Describe the morphology of the erythrocytes.
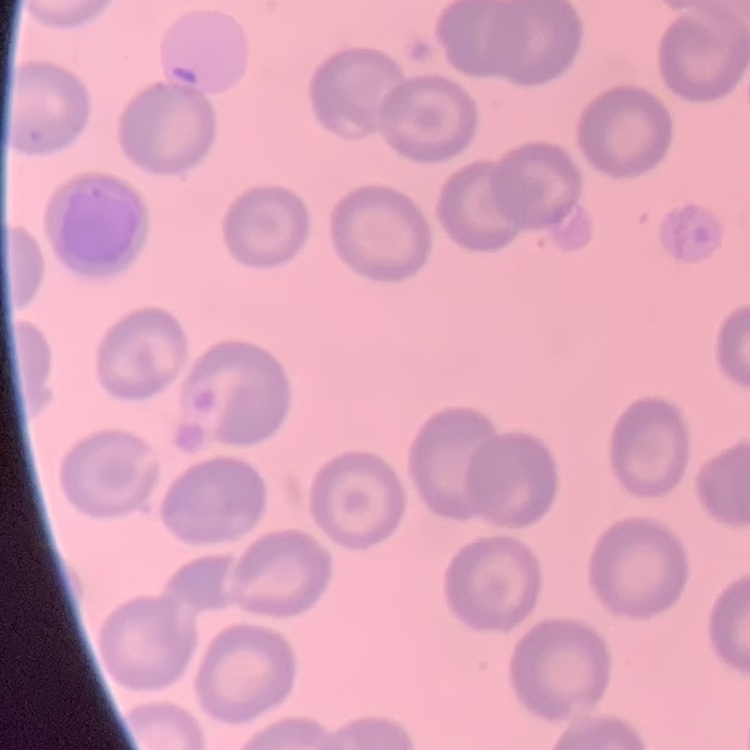
They show no rouleaux formation.

image_type: square crop of a larger photomicrograph
preparation: thin peripheral smear
stain: Field's or Giemsa